State which parasite is depicted.
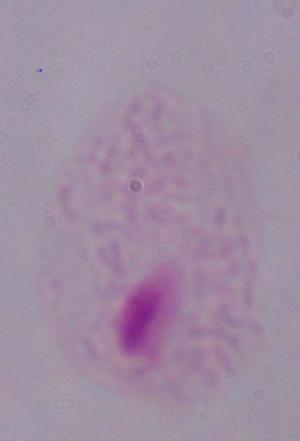
This is a trichomonad.

Captured at 1000x magnification. Photomicrograph.